Assess this cell for malaria.
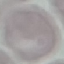
Uninfected.

preparation = thin blood film
capture = smartphone camera at the microscope eyepiece
image type = automatically extracted cell patch, resized to 64 × 64 pixels
stain = Giemsa